Locate every white blood cell.
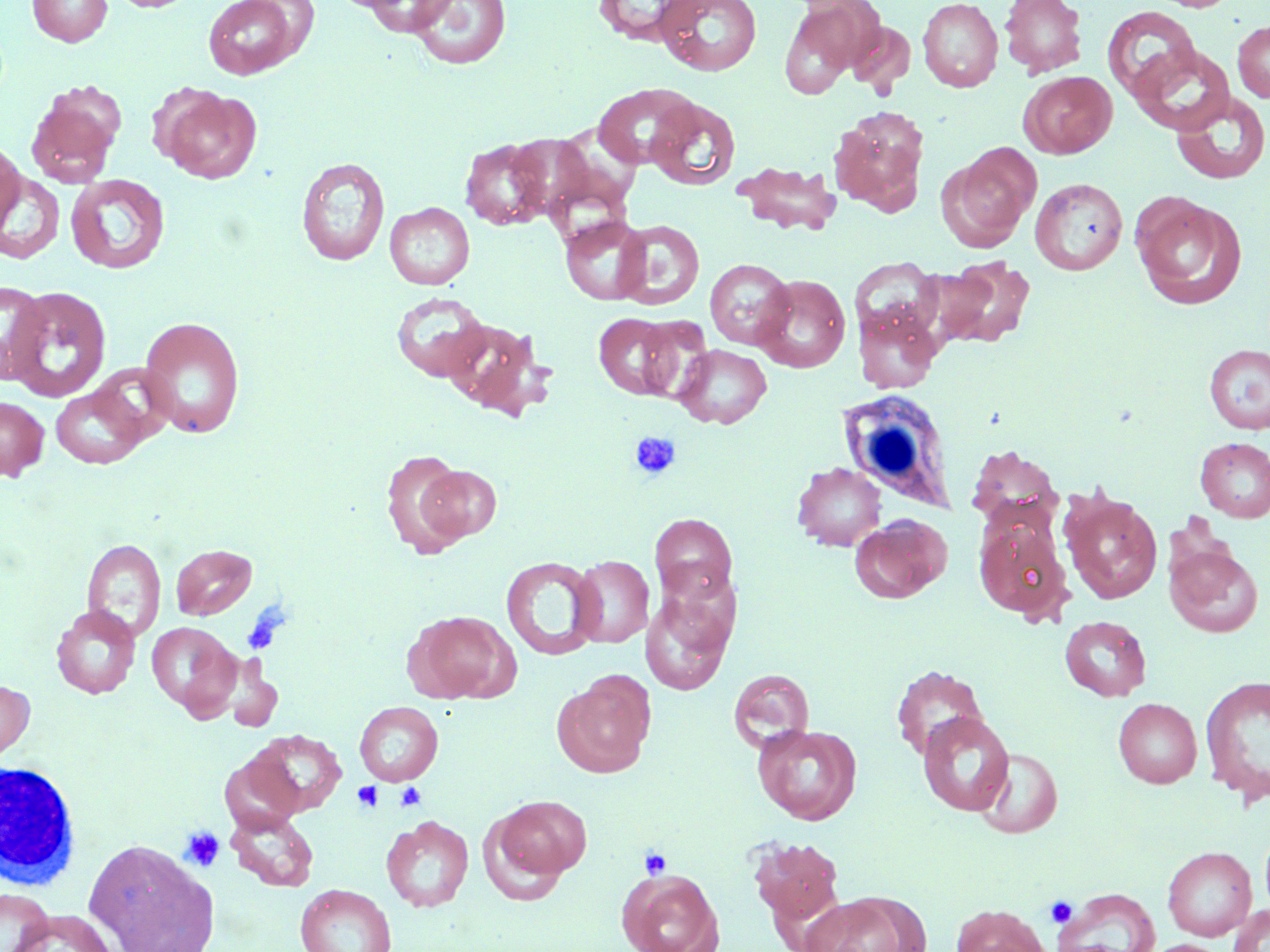

Approximate bounding boxes as (x1, y1, x2, y2) in pixels.
White blood cells: (835, 389, 957, 512), (1, 760, 83, 890).

Summary:
  - Platelet locations: (630, 432, 681, 479), (351, 781, 383, 812), (395, 782, 427, 811), (179, 827, 225, 872), (639, 848, 672, 880), (1046, 897, 1077, 928)
  - Uninfected red blood cell locations: (27, 0, 112, 47), (106, 0, 199, 13), (201, 0, 309, 79), (360, 0, 457, 37), (592, 0, 701, 46), (654, 0, 763, 76), (918, 0, 1003, 92), (999, 0, 1087, 78), (407, 1, 512, 70), (778, 1, 874, 99), (1102, 6, 1202, 105), (846, 20, 916, 94), (1232, 22, 1270, 102), (1129, 42, 1235, 134), (1019, 71, 1117, 158), (593, 84, 699, 168), (26, 86, 123, 187), (157, 87, 261, 183), (1170, 91, 1270, 185), (646, 97, 741, 191), (829, 106, 929, 214), (460, 138, 551, 230), (0, 140, 24, 232), (939, 148, 1037, 251), (296, 157, 390, 266), (732, 160, 842, 236), (0, 171, 65, 264), (65, 174, 170, 274), (1030, 178, 1128, 275), (1131, 194, 1246, 309), (385, 202, 474, 290), (560, 215, 653, 306), (614, 220, 704, 310), (937, 257, 1035, 348), (705, 259, 795, 349), (851, 260, 942, 344), (753, 274, 851, 373), (1, 280, 51, 383), (4, 286, 112, 403), (391, 292, 490, 382), (853, 303, 942, 393), (593, 312, 682, 400), (138, 315, 246, 438), (634, 316, 714, 402), (444, 319, 555, 422), (1204, 343, 1270, 434), (674, 344, 771, 428), (51, 385, 149, 468), (0, 395, 49, 481), (1195, 437, 1270, 522), (967, 444, 1063, 527), (381, 448, 473, 559), (417, 462, 502, 545), (792, 462, 886, 550), (1061, 490, 1162, 604), (649, 514, 737, 604), (850, 514, 951, 604), (973, 517, 1071, 620), (82, 538, 166, 642), (1164, 541, 1263, 637), (170, 543, 257, 620), (571, 555, 654, 647), (500, 556, 603, 660), (641, 584, 737, 696), (51, 604, 141, 699), (406, 610, 518, 703), (1060, 615, 1151, 701), (147, 622, 240, 717), (221, 654, 283, 732), (891, 664, 988, 761), (728, 668, 815, 753), (554, 673, 654, 777), (1200, 674, 1270, 804), (0, 677, 35, 773), (1113, 698, 1202, 788), (354, 701, 443, 786), (918, 712, 1014, 816), (752, 723, 862, 825), (248, 729, 348, 816), (977, 747, 1063, 838), (220, 753, 304, 834), (492, 795, 591, 881), (226, 810, 318, 891), (381, 815, 474, 912), (748, 837, 845, 928), (84, 838, 219, 952), (1162, 846, 1257, 940), (617, 868, 724, 952), (295, 884, 396, 952), (1051, 886, 1160, 952), (0, 887, 54, 952), (800, 892, 925, 952), (1227, 903, 1270, 952), (950, 904, 1051, 952), (9, 908, 116, 952), (1142, 939, 1228, 952)
  - Slide-level diagnosis: negative for blood parasites
  - Modality: light microscopy
  - Magnification: 1000x
  - Preparation: thin blood smear
  - Image size: 1270×952 pixels
  - Stain: May-Grünwald-Giemsa
  - Field of view: single